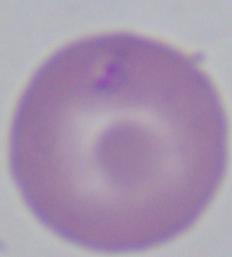

{
  "magnification": "1000x",
  "identification": "Babesia",
  "modality": "micrograph"
}